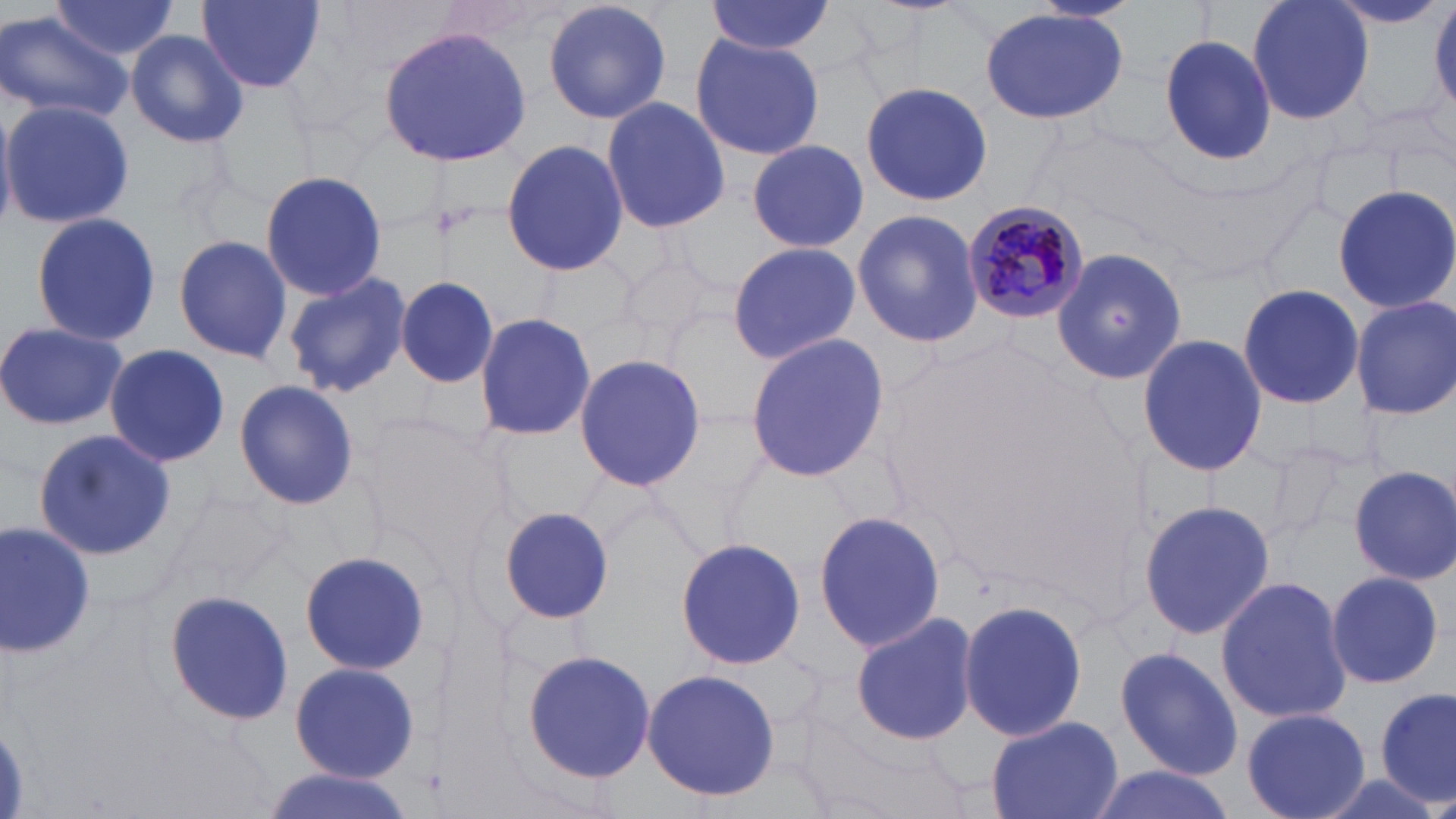 Approximate bounding boxes as named x1/y1/x2/y2 corners in pixels. Plasmodium malariae-infected red blood cell locations: (x1=964, y1=199, x2=1091, y2=325). Uninfected red blood cell locations: (x1=194, y1=0, x2=330, y2=96), (x1=705, y1=0, x2=837, y2=57), (x1=1246, y1=0, x2=1375, y2=127), (x1=1430, y1=0, x2=1456, y2=114), (x1=543, y1=1, x2=673, y2=127), (x1=46, y1=2, x2=183, y2=61), (x1=1325, y1=2, x2=1450, y2=31), (x1=979, y1=6, x2=1131, y2=126), (x1=0, y1=10, x2=134, y2=125), (x1=378, y1=25, x2=530, y2=168), (x1=123, y1=30, x2=250, y2=149), (x1=689, y1=31, x2=826, y2=162), (x1=1157, y1=32, x2=1278, y2=166), (x1=859, y1=81, x2=993, y2=206), (x1=600, y1=97, x2=731, y2=233), (x1=1, y1=100, x2=137, y2=229), (x1=499, y1=138, x2=629, y2=278), (x1=745, y1=139, x2=870, y2=254), (x1=259, y1=168, x2=388, y2=302), (x1=1332, y1=184, x2=1456, y2=316), (x1=851, y1=208, x2=985, y2=348), (x1=29, y1=210, x2=161, y2=349), (x1=173, y1=236, x2=293, y2=362), (x1=725, y1=242, x2=861, y2=363), (x1=1052, y1=245, x2=1186, y2=387), (x1=282, y1=271, x2=412, y2=398), (x1=395, y1=278, x2=502, y2=386), (x1=1237, y1=283, x2=1363, y2=410), (x1=1350, y1=296, x2=1456, y2=419), (x1=475, y1=311, x2=596, y2=443), (x1=0, y1=322, x2=128, y2=430), (x1=743, y1=332, x2=889, y2=482), (x1=1137, y1=333, x2=1268, y2=478), (x1=104, y1=343, x2=229, y2=467), (x1=573, y1=350, x2=708, y2=493), (x1=233, y1=380, x2=360, y2=509), (x1=31, y1=429, x2=173, y2=559), (x1=1349, y1=466, x2=1455, y2=583), (x1=1137, y1=499, x2=1276, y2=638), (x1=497, y1=504, x2=619, y2=627), (x1=812, y1=510, x2=948, y2=654), (x1=0, y1=520, x2=97, y2=658), (x1=674, y1=537, x2=810, y2=668), (x1=299, y1=549, x2=430, y2=678), (x1=1323, y1=572, x2=1449, y2=689), (x1=1214, y1=576, x2=1353, y2=726), (x1=163, y1=589, x2=295, y2=725), (x1=957, y1=599, x2=1088, y2=740), (x1=852, y1=612, x2=981, y2=746), (x1=1114, y1=645, x2=1244, y2=779), (x1=522, y1=648, x2=657, y2=784), (x1=289, y1=662, x2=419, y2=783), (x1=643, y1=669, x2=780, y2=801), (x1=1374, y1=689, x2=1454, y2=806), (x1=1240, y1=706, x2=1373, y2=819), (x1=986, y1=714, x2=1124, y2=819), (x1=1082, y1=765, x2=1242, y2=819), (x1=258, y1=769, x2=414, y2=819). Slide-level diagnosis: Plasmodium malariae. Thin blood smear. Light microscopy. 1000x magnification. Single field of view. May-Grünwald-Giemsa stain. Image is 1456×819 pixels.